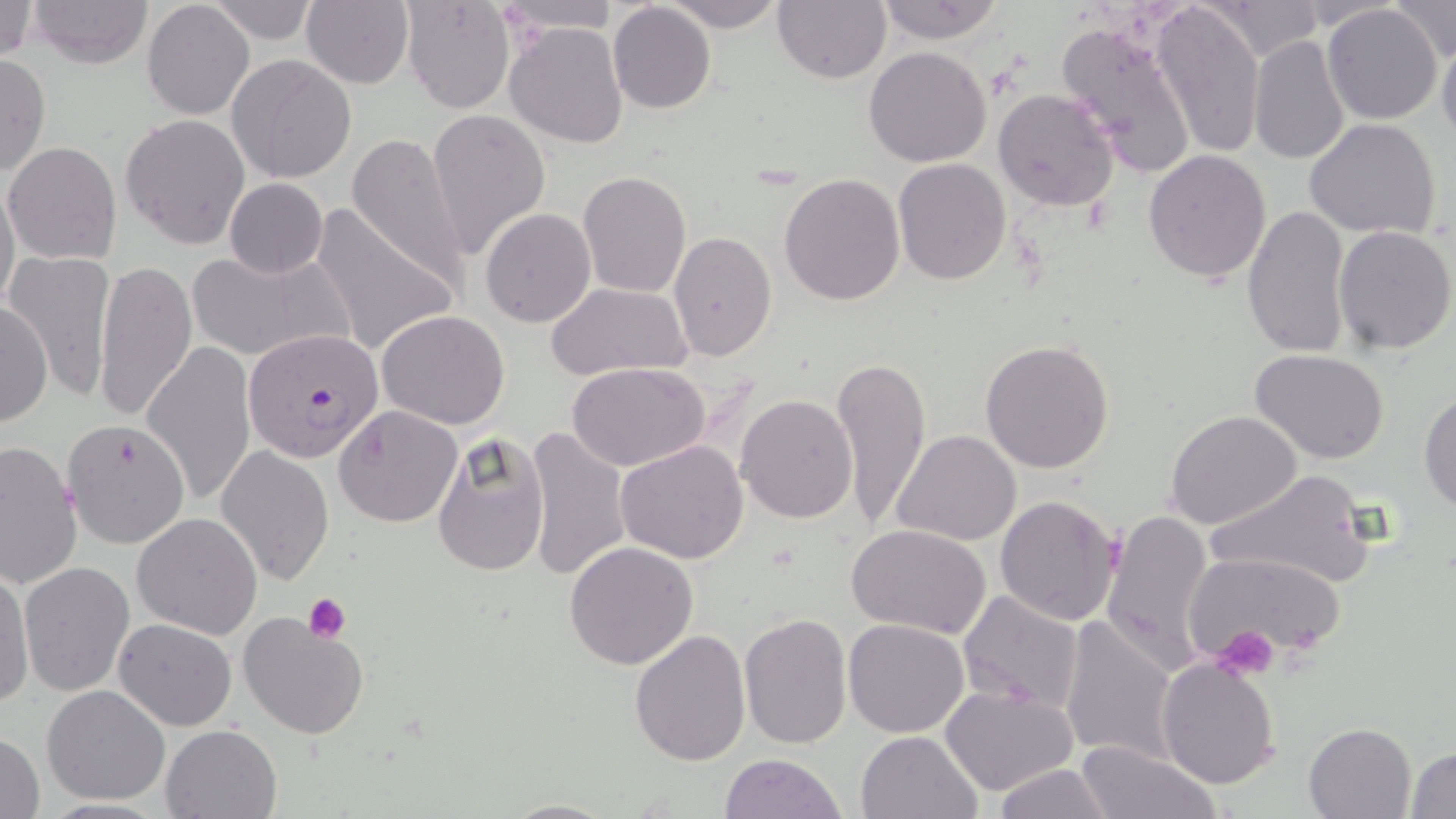
{
  "slide_level_diagnosis": "Plasmodium falciparum",
  "magnification": "1000x",
  "modality": "light microscopy",
  "uninfected_red_blood_cell_locations": "approximate bounding boxes as (x1,y1)-(x2,y2) corner pairs in pixels: (26,0)-(154,68), (301,0)-(415,89), (400,0)-(516,113), (493,0)-(622,35), (659,0)-(789,30), (772,0)-(890,85), (1387,0)-(1455,64), (0,1)-(39,64), (142,1)-(255,121), (205,1)-(322,47), (873,1)-(1009,45), (1152,1)-(1265,160), (607,2)-(715,114), (1208,2)-(1319,61), (1322,5)-(1442,125), (1053,17)-(1199,177), (504,21)-(629,150), (1245,22)-(1437,150), (1436,30)-(1456,143), (1248,36)-(1350,169), (864,46)-(993,167), (0,52)-(50,181), (225,54)-(357,185), (992,86)-(1121,214), (428,107)-(549,258), (120,114)-(252,250), (1304,117)-(1442,241), (346,135)-(474,290), (3,141)-(121,264), (1142,149)-(1272,285), (893,158)-(1012,283), (576,170)-(691,298), (779,173)-(906,305), (0,175)-(21,318), (223,178)-(328,278), (307,203)-(460,359), (1242,204)-(1352,360), (480,208)-(597,329), (1332,225)-(1455,355), (667,232)-(776,361), (185,248)-(352,365), (3,250)-(118,402), (93,258)-(197,425), (544,280)-(693,383), (0,301)-(51,429), (377,309)-(511,428), (979,338)-(1115,474), (142,341)-(257,507), (1250,348)-(1392,463), (831,354)-(933,532), (569,362)-(710,470), (1418,388)-(1456,514), (733,393)-(858,524), (334,405)-(463,528), (1166,410)-(1303,530), (65,415)-(192,551), (522,426)-(634,582), (893,429)-(1023,548), (432,433)-(550,578), (0,439)-(83,591), (615,441)-(749,565), (216,444)-(334,586), (1204,466)-(1380,593), (994,495)-(1123,626), (1102,509)-(1215,673), (132,513)-(262,639), (847,525)-(990,639), (564,541)-(698,669), (1182,551)-(1349,673), (19,560)-(136,697), (0,572)-(34,707), (958,589)-(1086,716), (237,610)-(370,740), (739,611)-(852,748), (1058,615)-(1179,767), (114,618)-(237,730), (841,619)-(970,738), (628,628)-(750,765), (1155,657)-(1281,791), (41,684)-(171,806), (938,684)-(1079,798), (1303,721)-(1418,818), (161,724)-(283,818), (855,729)-(982,819), (0,732)-(46,818), (1074,740)-(1222,818), (1407,745)-(1456,817), (719,753)-(849,819), (989,763)-(1116,818), (496,798)-(623,818)",
  "preparation": "thin blood smear",
  "plasmodium_falciparum_infected_red_blood_cell_locations": "approximate bounding boxes as (x1,y1)-(x2,y2) corner pairs in pixels: (247,332)-(385,457)",
  "stain": "May-Grünwald-Giemsa",
  "platelet_locations": "approximate bounding boxes as (x1,y1)-(x2,y2) corner pairs in pixels: (303,593)-(351,644), (1215,625)-(1283,678)",
  "field_of_view": "one of a larger specimen",
  "image_size": "1456×819 pixels"
}